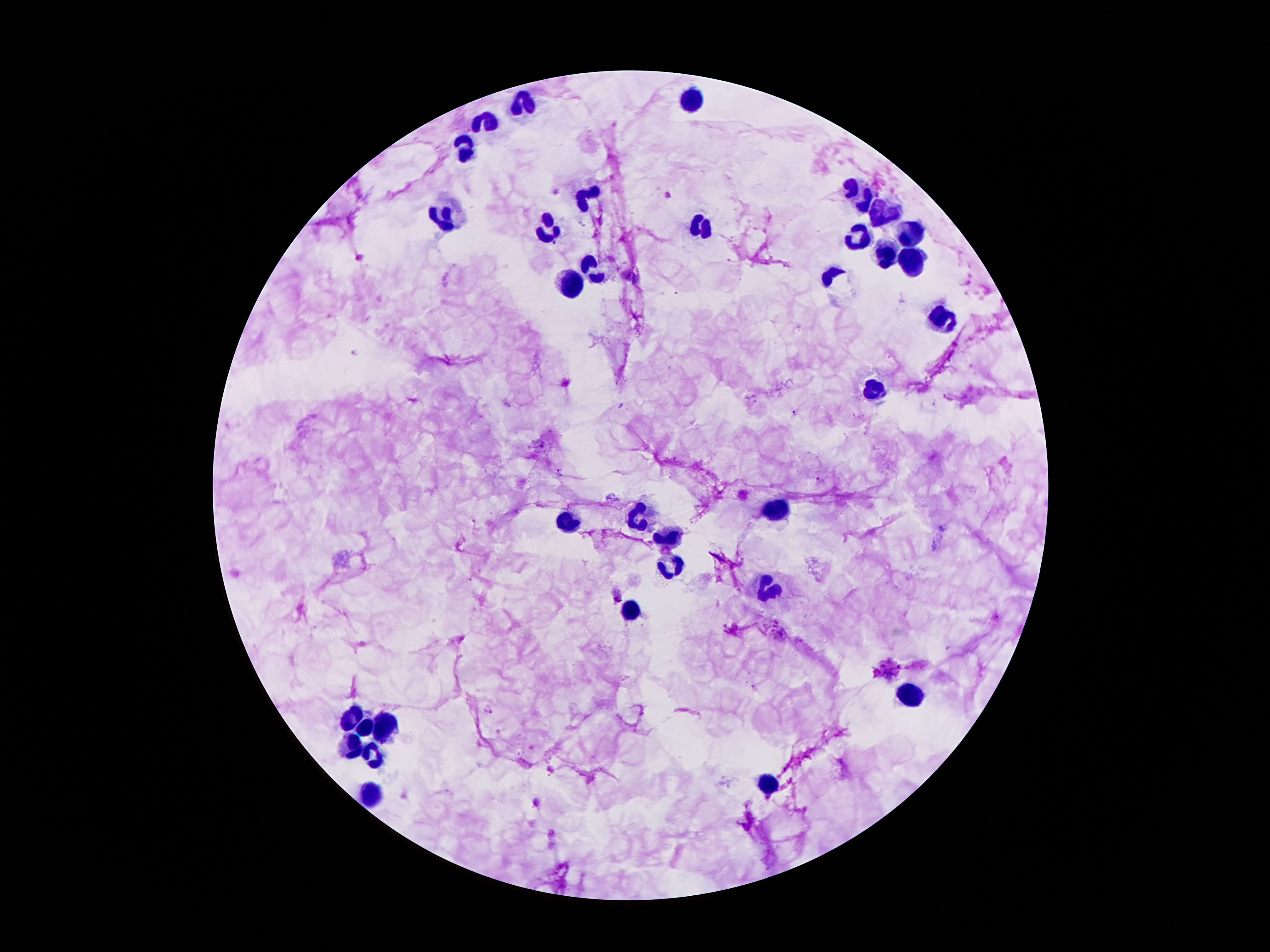

Approximate centers as [x, y] in pixels.
Summary:
  - Leukocyte locations: [690, 101], [520, 106], [487, 122], [464, 149], [852, 187], [593, 195], [862, 204], [884, 213], [446, 215], [703, 228], [548, 230], [910, 235], [858, 241], [888, 256], [912, 256], [585, 266], [571, 284], [944, 318], [873, 394], [776, 512], [569, 523], [636, 523], [666, 541], [673, 569], [768, 590], [632, 615], [908, 696], [350, 718], [386, 725], [365, 729], [350, 748], [375, 754], [774, 780], [371, 795]
  - Plasmodium parasite locations: [623, 406], [796, 414], [560, 472], [619, 596], [486, 709]
  - Patient malaria status: infected with Plasmodium falciparum
  - Magnification: 100x
  - Stain: Giemsa
  - Preparation: thick blood smear
  - Capture: smartphone through the microscope eyepiece
  - Field of view: single
  - Image size: 1270×952 pixels